Assess this cell for malaria.
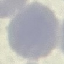

It is uninfected.

{
  "capture": "smartphone through the microscope eyepiece",
  "preparation": "thin blood film",
  "stain": "Giemsa",
  "image_type": "automatically extracted cell patch, resized to 64 × 64 pixels"
}